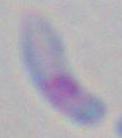

Toxoplasma gondii is shown. Micrograph. 1000x magnification.